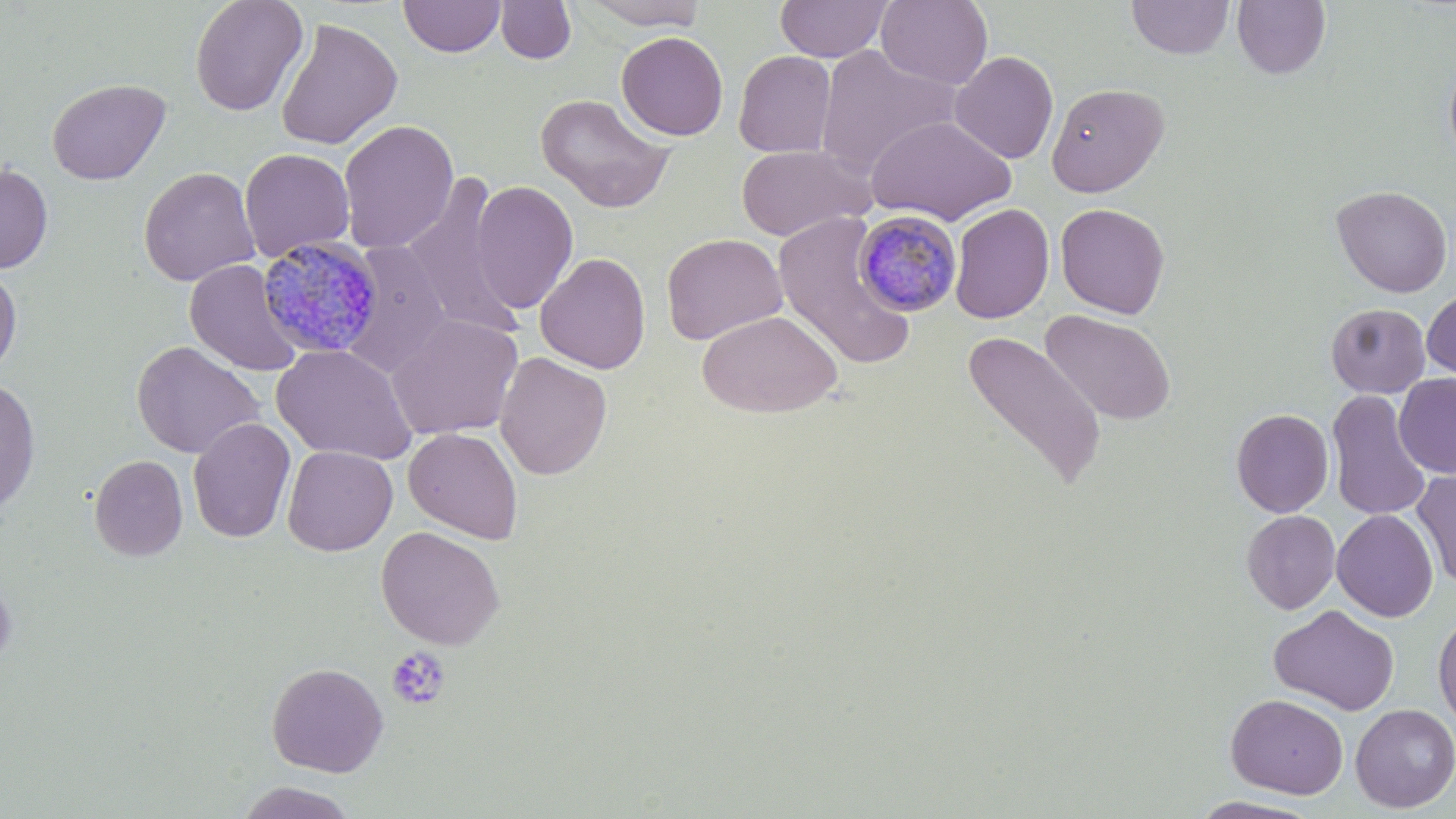 Approximate bounding boxes as (x1, y1, x2, y2) in pixels. Platelet locations: (386, 647, 451, 710). Plasmodium malariae-infected red blood cell locations: (851, 210, 962, 315), (261, 235, 382, 360). Uninfected red blood cell locations: (188, 0, 309, 117), (398, 0, 505, 58), (581, 0, 708, 30), (775, 0, 893, 62), (876, 0, 993, 89), (1126, 0, 1235, 60), (494, 1, 577, 64), (1232, 1, 1331, 79), (275, 17, 402, 150), (616, 31, 728, 140), (814, 45, 961, 178), (733, 50, 837, 158), (950, 50, 1059, 164), (1443, 51, 1456, 169), (46, 78, 170, 185), (1046, 82, 1169, 197), (535, 93, 676, 214), (865, 115, 1016, 226), (338, 119, 459, 254), (735, 144, 873, 241), (239, 148, 355, 262), (0, 163, 53, 273), (138, 167, 260, 287), (400, 174, 523, 340), (471, 181, 579, 314), (1331, 185, 1453, 298), (949, 203, 1055, 324), (1055, 203, 1171, 318), (772, 212, 918, 370), (661, 233, 787, 344), (341, 241, 453, 378), (535, 252, 651, 374), (185, 259, 304, 376), (0, 264, 23, 377), (1422, 288, 1456, 384), (1326, 303, 1431, 398), (696, 309, 842, 418), (1041, 309, 1177, 426), (387, 314, 523, 440), (961, 331, 1108, 493), (131, 341, 265, 459), (271, 344, 417, 465), (494, 351, 613, 480), (1394, 374, 1456, 478), (0, 376, 41, 513), (1326, 391, 1433, 522), (1231, 409, 1333, 517), (187, 417, 296, 543), (404, 427, 523, 544), (281, 438, 522, 550), (282, 445, 398, 556), (89, 455, 188, 560), (1411, 471, 1456, 589), (1332, 509, 1438, 622), (1241, 510, 1340, 614), (375, 526, 505, 649), (0, 569, 16, 673), (1268, 604, 1400, 716), (1433, 613, 1456, 729), (266, 662, 388, 776), (1226, 693, 1348, 798), (1350, 703, 1456, 813), (235, 781, 359, 818), (1188, 795, 1325, 818). Slide-level diagnosis: Plasmodium malariae. Thin blood smear. 1000x magnification. Single field of view. Image is 1456×819 pixels. May-Grünwald-Giemsa-stained preparation. Optical microscopy.